Assess the morphology of the red blood cells.
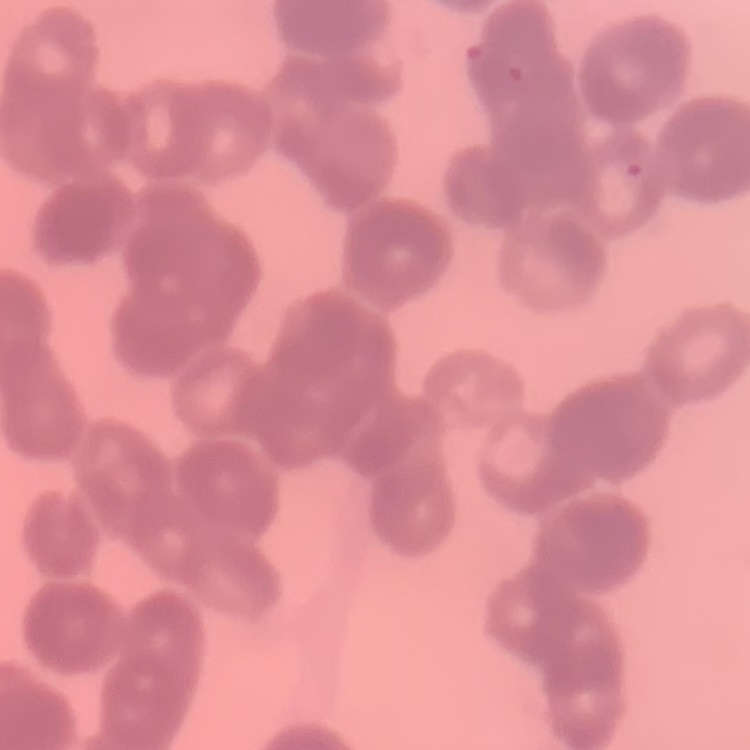

Rouleaux formation.

Stained with either Field's or Giemsa. Square crop of a larger photomicrograph. Thin blood smear.